Identify the cell.
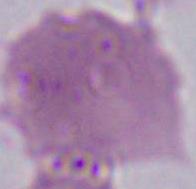

This is an erythrocyte.

Micrograph. 1000x magnification.